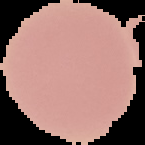

Malaria status: uninfected. The area outside the segmented cell region is set to black. From a thin blood film. Image is 145×145 pixels.